Assess the morphology of the erythrocytes.
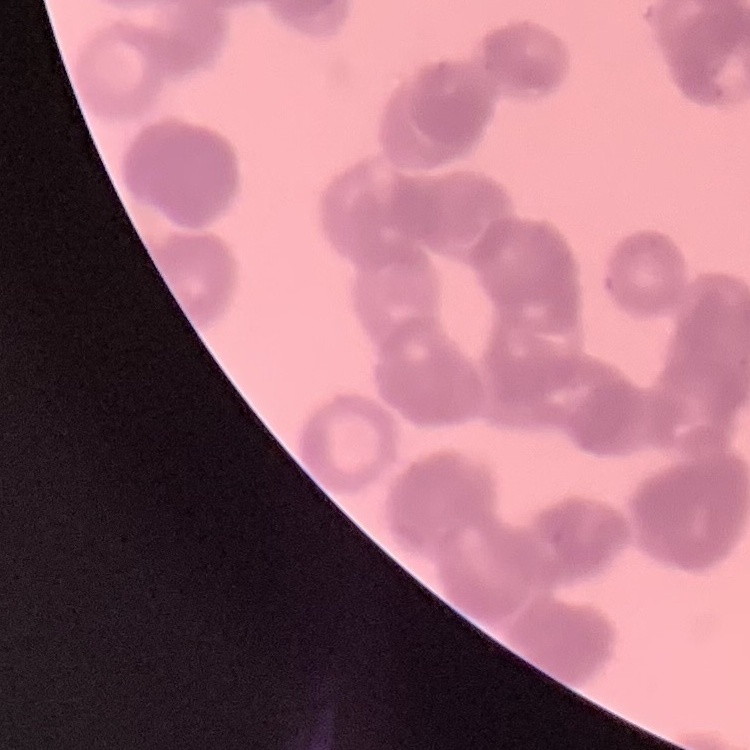

They show rouleaux formation.

Summary:
  - Image type: one tile cut from a larger photomicrograph
  - Preparation: thin blood smear
  - Stain: Field's or Giemsa